Assess the morphology of the erythrocytes.
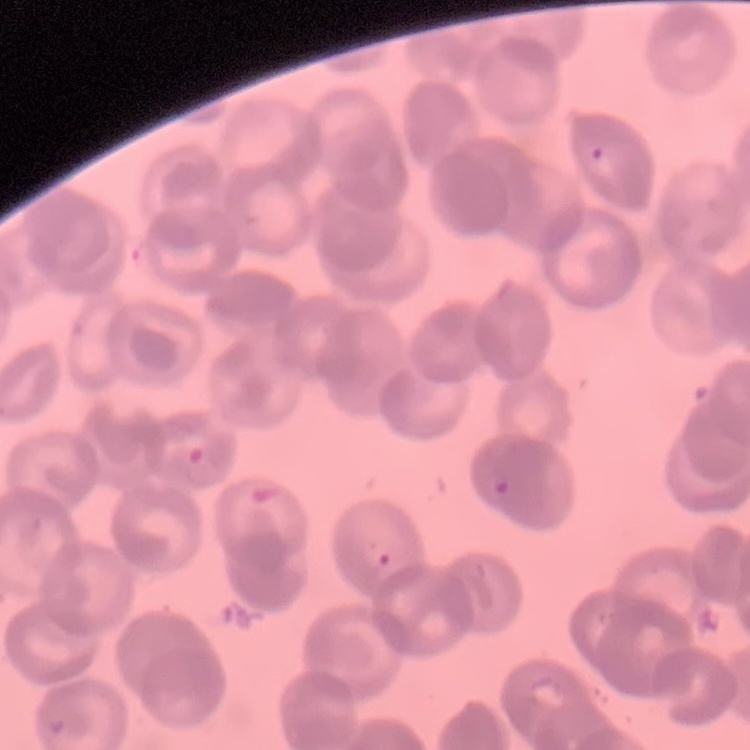

They show rouleaux formation.

stain = Field's or Giemsa
preparation = thin peripheral smear
image type = square crop of a larger photomicrograph